Name the cell type shown.
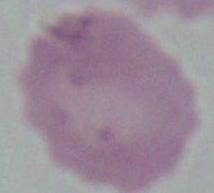
This is an erythrocyte.

Photomicrograph. 1000x magnification.